Locate every blood parasite and identify its species.
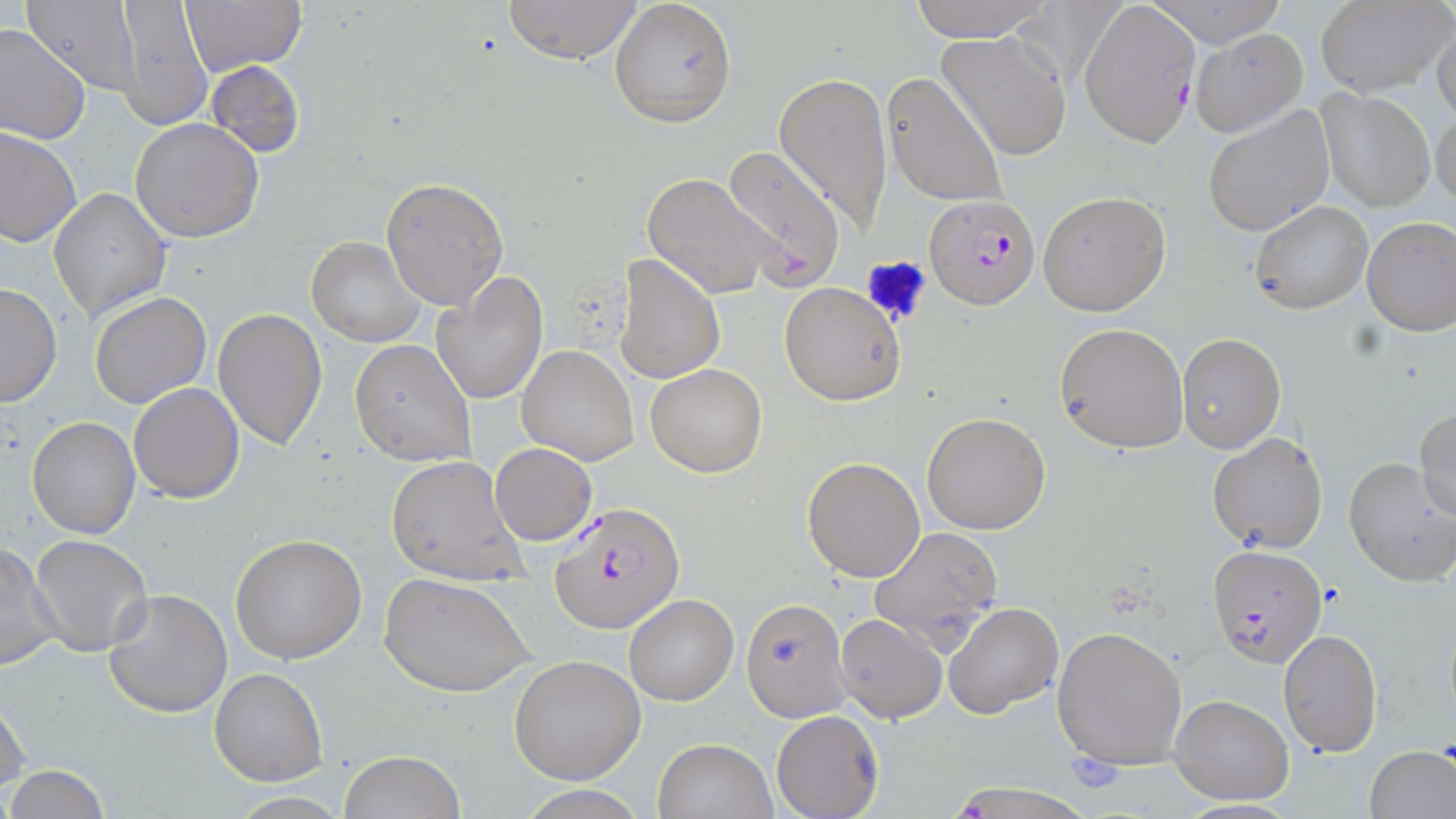

Approximate bounding boxes as named x1/y1/x2/y2 corners in pixels.
Plasmodium falciparum-infected red blood cells: (x1=1081, y1=2, x2=1199, y2=147), (x1=925, y1=194, x2=1039, y2=310), (x1=549, y1=502, x2=684, y2=635), (x1=1207, y1=543, x2=1328, y2=667).
No Plasmodium ovale, Plasmodium malariae, Plasmodium vivax, Babesia divergens, or Trypanosoma brucei observed.

Uninfected red blood cell locations: (x1=177, y1=0, x2=307, y2=77), (x1=501, y1=0, x2=646, y2=67), (x1=905, y1=0, x2=1058, y2=43), (x1=1146, y1=0, x2=1288, y2=47), (x1=22, y1=1, x2=142, y2=96), (x1=113, y1=1, x2=212, y2=131), (x1=610, y1=1, x2=736, y2=128), (x1=1317, y1=1, x2=1453, y2=95), (x1=1431, y1=22, x2=1456, y2=124), (x1=0, y1=23, x2=90, y2=145), (x1=1190, y1=29, x2=1308, y2=136), (x1=936, y1=32, x2=1072, y2=160), (x1=205, y1=58, x2=306, y2=159), (x1=775, y1=71, x2=892, y2=228), (x1=882, y1=72, x2=1007, y2=208), (x1=1315, y1=87, x2=1435, y2=211), (x1=1431, y1=103, x2=1455, y2=210), (x1=1202, y1=104, x2=1335, y2=237), (x1=130, y1=118, x2=264, y2=243), (x1=0, y1=126, x2=80, y2=248), (x1=721, y1=148, x2=846, y2=289), (x1=640, y1=172, x2=780, y2=299), (x1=381, y1=176, x2=508, y2=309), (x1=48, y1=187, x2=172, y2=322), (x1=1037, y1=190, x2=1170, y2=315), (x1=1248, y1=201, x2=1373, y2=316), (x1=1361, y1=216, x2=1456, y2=337), (x1=307, y1=238, x2=424, y2=348), (x1=617, y1=254, x2=724, y2=386), (x1=432, y1=272, x2=548, y2=405), (x1=779, y1=281, x2=908, y2=405), (x1=0, y1=283, x2=61, y2=408), (x1=89, y1=292, x2=211, y2=410), (x1=212, y1=308, x2=327, y2=451), (x1=1055, y1=322, x2=1189, y2=452), (x1=1177, y1=333, x2=1286, y2=454), (x1=348, y1=339, x2=476, y2=466), (x1=516, y1=345, x2=638, y2=466), (x1=646, y1=363, x2=766, y2=477), (x1=129, y1=383, x2=246, y2=502), (x1=1414, y1=408, x2=1456, y2=524), (x1=922, y1=412, x2=1051, y2=535), (x1=27, y1=416, x2=141, y2=539), (x1=1207, y1=432, x2=1329, y2=554), (x1=489, y1=443, x2=598, y2=547), (x1=386, y1=455, x2=524, y2=584), (x1=803, y1=457, x2=926, y2=582), (x1=1344, y1=457, x2=1456, y2=586), (x1=868, y1=526, x2=1005, y2=649), (x1=230, y1=533, x2=368, y2=664), (x1=30, y1=534, x2=153, y2=656), (x1=0, y1=542, x2=62, y2=671), (x1=380, y1=573, x2=534, y2=698), (x1=102, y1=588, x2=234, y2=719), (x1=625, y1=594, x2=739, y2=706), (x1=740, y1=595, x2=851, y2=720), (x1=945, y1=603, x2=1063, y2=719), (x1=836, y1=614, x2=947, y2=723), (x1=1052, y1=623, x2=1188, y2=770), (x1=1279, y1=629, x2=1385, y2=757), (x1=509, y1=655, x2=646, y2=784), (x1=211, y1=668, x2=326, y2=785), (x1=1169, y1=694, x2=1294, y2=805), (x1=0, y1=696, x2=31, y2=796), (x1=771, y1=710, x2=883, y2=819), (x1=652, y1=737, x2=777, y2=818), (x1=1365, y1=745, x2=1456, y2=819), (x1=339, y1=751, x2=465, y2=819), (x1=5, y1=765, x2=113, y2=818), (x1=943, y1=782, x2=1101, y2=817), (x1=515, y1=785, x2=650, y2=818). Platelet locations: (x1=860, y1=254, x2=932, y2=327), (x1=1067, y1=753, x2=1124, y2=793). Slide-level diagnosis: Plasmodium falciparum. 1000x magnification. Optical microscopy. Thin blood film. Image is 1456×819 pixels. May-Grünwald-Giemsa-stained preparation. Single field of view.